Assess this cell for malaria.
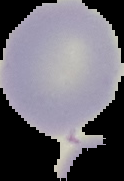
It is uninfected.

The area outside the segmented cell region is set to black. Image is 124×181 pixels. From a thin blood smear.